Identify the parasite.
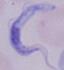

A trypanosome.

modality = micrograph
magnification = 1000x